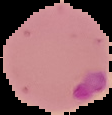

preparation = thin blood smear
image size = 112×115 pixels
image type = segmented cell region with the area outside set to black
malaria status = parasitized